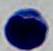
A leukocyte is seen. 1000x magnification. Micrograph.